Identify the parasite.
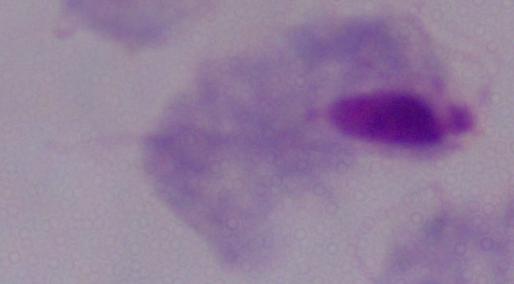

A trichomonad.

modality = micrograph
magnification = 1000x